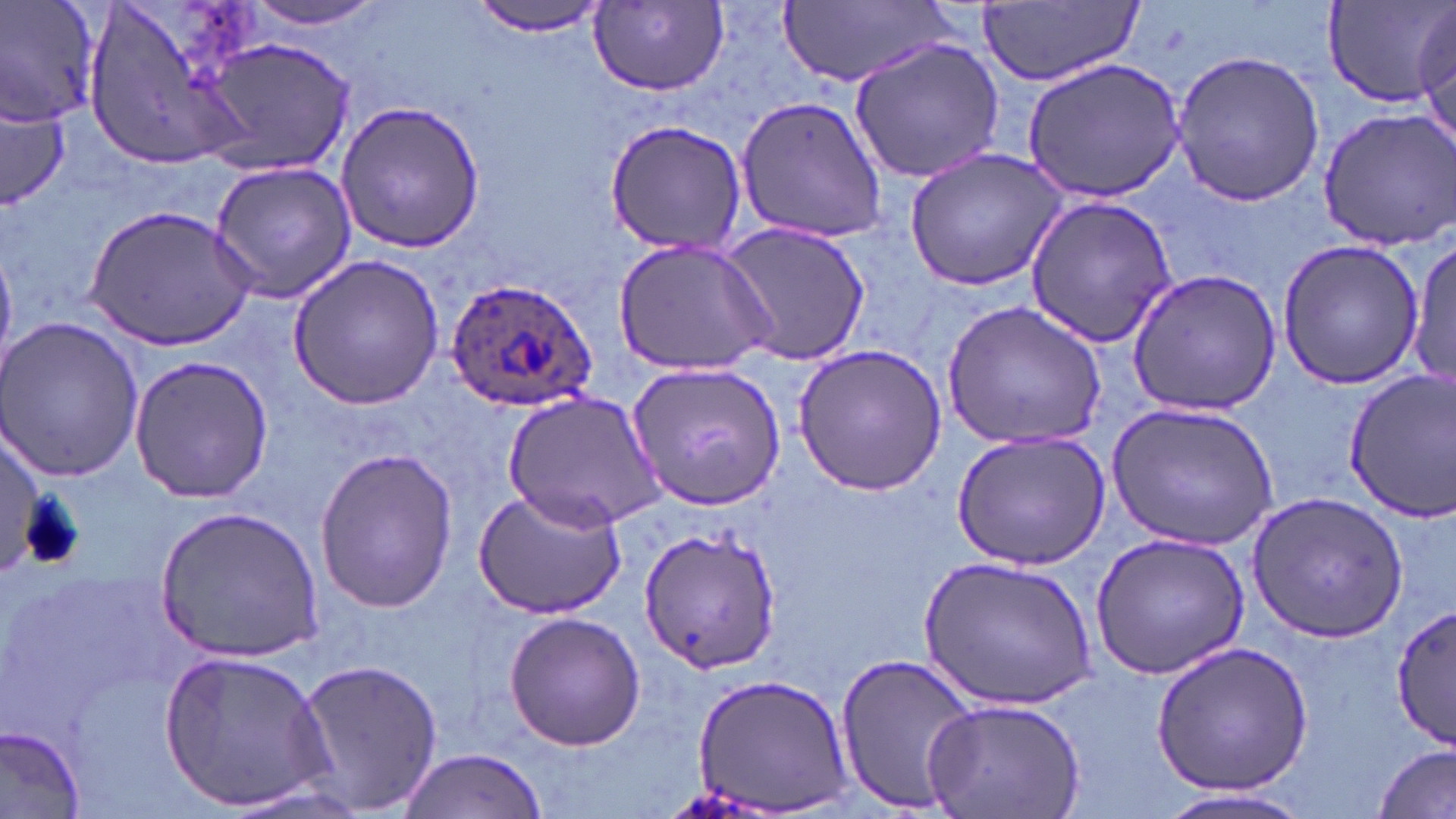

Summary:
  - Coordinate format: approximate bounding boxes as (x1,y1)-(x2,y2) corner pairs in pixels
  - Uninfected red blood cell locations: (0,0)-(100,127), (81,0)-(265,171), (240,0)-(394,31), (467,0)-(612,38), (777,0)-(954,91), (1323,1)-(1456,106), (978,2)-(1142,87), (591,3)-(729,96), (201,37)-(353,175), (848,39)-(1007,182), (1170,49)-(1324,205), (1022,59)-(1185,200), (735,92)-(890,243), (0,96)-(69,208), (337,101)-(485,255), (1316,107)-(1456,249), (602,118)-(751,257), (903,148)-(1070,292), (208,161)-(356,303), (1024,194)-(1179,346), (82,202)-(258,350), (719,222)-(870,368), (1408,232)-(1456,391), (613,237)-(778,378), (1274,239)-(1425,389), (286,252)-(445,411), (1125,268)-(1283,417), (943,299)-(1108,450), (0,314)-(146,483), (792,343)-(948,496), (128,354)-(273,505), (626,362)-(784,510), (1342,367)-(1456,523), (502,389)-(665,530), (1105,400)-(1284,551), (952,430)-(1111,567), (1,435)-(47,575), (310,448)-(462,611), (473,485)-(628,620), (1245,491)-(1407,643), (152,505)-(326,664), (638,526)-(778,676), (1088,530)-(1250,679), (920,555)-(1100,711), (1388,597)-(1454,752), (503,611)-(644,751), (1148,639)-(1314,797), (158,648)-(334,813), (833,652)-(981,813), (293,657)-(445,816), (689,672)-(855,811), (922,696)-(1089,819), (0,724)-(84,816), (1376,743)-(1455,818), (394,750)-(550,819), (1145,786)-(1318,819)
  - Plasmodium ovale-infected red blood cell locations: (443,276)-(599,411)
  - Slide-level diagnosis: Plasmodium ovale
  - Magnification: 1000x
  - Field of view: one of a larger specimen
  - Preparation: thin blood smear
  - Image size: 1456×819 pixels
  - Modality: light microscopy
  - Stain: May-Grünwald-Giemsa